Identify the parasite.
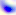

This is Toxoplasma gondii.

Summary:
  - Magnification: 400x
  - Modality: photomicrograph